State which parasite is depicted.
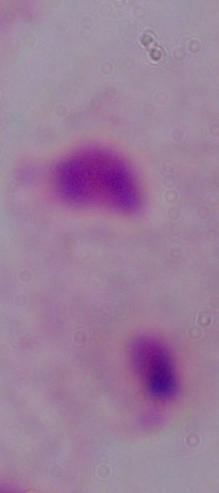
A trichomonad.

magnification = 1000x
modality = photomicrograph